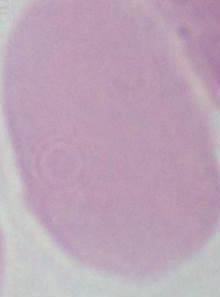
magnification = 1000x
identification = red blood cell
modality = micrograph